Assess this cell for malaria.
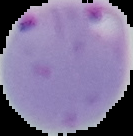

Parasitized.

Image is 133×136 pixels. From a thin blood film. The area outside the segmented cell region is set to black.